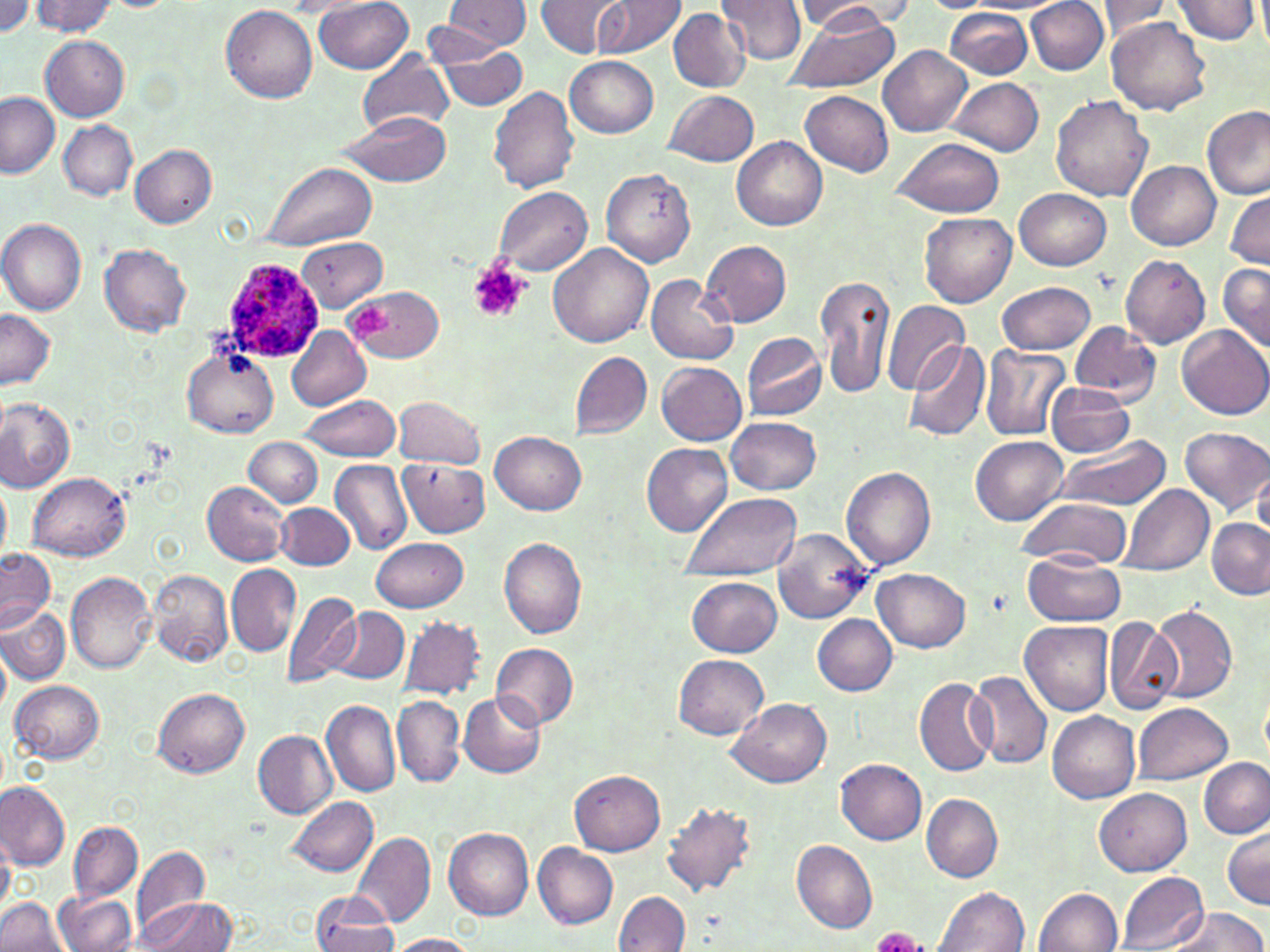
Summary:
  - Coordinate format: approximate bounding boxes as named x1/y1/x2/y2 corners in pixels
  - Platelet locations: (x1=468, y1=261, x2=530, y2=324), (x1=346, y1=300, x2=392, y2=344), (x1=871, y1=925, x2=927, y2=952)
  - Plasmodium ovale-infected red blood cell locations: (x1=220, y1=255, x2=321, y2=365)
  - Uninfected red blood cell locations: (x1=0, y1=0, x2=34, y2=36), (x1=314, y1=0, x2=413, y2=74), (x1=536, y1=0, x2=629, y2=58), (x1=594, y1=0, x2=684, y2=59), (x1=717, y1=0, x2=808, y2=68), (x1=792, y1=0, x2=915, y2=34), (x1=1027, y1=0, x2=1108, y2=75), (x1=1169, y1=0, x2=1263, y2=45), (x1=30, y1=1, x2=124, y2=37), (x1=441, y1=1, x2=533, y2=50), (x1=925, y1=1, x2=991, y2=13), (x1=1093, y1=2, x2=1176, y2=39), (x1=220, y1=5, x2=317, y2=104), (x1=668, y1=9, x2=752, y2=92), (x1=780, y1=10, x2=899, y2=94), (x1=946, y1=10, x2=1034, y2=80), (x1=1106, y1=16, x2=1210, y2=116), (x1=39, y1=34, x2=129, y2=121), (x1=428, y1=37, x2=530, y2=111), (x1=879, y1=45, x2=972, y2=136), (x1=358, y1=49, x2=452, y2=134), (x1=565, y1=56, x2=658, y2=137), (x1=948, y1=77, x2=1044, y2=156), (x1=489, y1=86, x2=581, y2=194), (x1=664, y1=90, x2=760, y2=167), (x1=802, y1=90, x2=894, y2=176), (x1=0, y1=92, x2=60, y2=179), (x1=1051, y1=95, x2=1152, y2=202), (x1=1200, y1=105, x2=1269, y2=200), (x1=336, y1=110, x2=452, y2=187), (x1=59, y1=122, x2=137, y2=199), (x1=891, y1=135, x2=1005, y2=219), (x1=732, y1=136, x2=829, y2=230), (x1=128, y1=144, x2=217, y2=228), (x1=262, y1=161, x2=377, y2=250), (x1=1128, y1=161, x2=1220, y2=249), (x1=601, y1=167, x2=696, y2=267), (x1=493, y1=187, x2=593, y2=274), (x1=1015, y1=187, x2=1110, y2=270), (x1=1225, y1=189, x2=1270, y2=270), (x1=920, y1=213, x2=1018, y2=308), (x1=0, y1=218, x2=86, y2=316), (x1=295, y1=237, x2=388, y2=313), (x1=700, y1=242, x2=792, y2=327), (x1=100, y1=244, x2=192, y2=337), (x1=548, y1=244, x2=653, y2=347), (x1=1120, y1=255, x2=1211, y2=348), (x1=1218, y1=263, x2=1270, y2=355), (x1=646, y1=273, x2=738, y2=366), (x1=817, y1=274, x2=896, y2=403), (x1=996, y1=282, x2=1098, y2=355), (x1=347, y1=287, x2=444, y2=363), (x1=882, y1=300, x2=970, y2=396), (x1=0, y1=309, x2=54, y2=390), (x1=1070, y1=320, x2=1161, y2=403), (x1=286, y1=325, x2=371, y2=410), (x1=1176, y1=325, x2=1270, y2=420), (x1=741, y1=332, x2=827, y2=422), (x1=903, y1=339, x2=992, y2=444), (x1=981, y1=344, x2=1072, y2=441), (x1=183, y1=348, x2=278, y2=436), (x1=568, y1=351, x2=653, y2=441), (x1=657, y1=362, x2=748, y2=446), (x1=1045, y1=382, x2=1134, y2=456), (x1=298, y1=394, x2=402, y2=462), (x1=394, y1=396, x2=485, y2=469), (x1=0, y1=397, x2=75, y2=492), (x1=726, y1=416, x2=822, y2=495), (x1=1179, y1=426, x2=1270, y2=515), (x1=490, y1=431, x2=587, y2=515), (x1=970, y1=436, x2=1070, y2=526), (x1=1051, y1=436, x2=1172, y2=510), (x1=246, y1=437, x2=324, y2=508), (x1=642, y1=442, x2=735, y2=536), (x1=398, y1=458, x2=490, y2=538), (x1=331, y1=459, x2=413, y2=557), (x1=841, y1=466, x2=938, y2=569), (x1=1253, y1=468, x2=1270, y2=540), (x1=28, y1=472, x2=131, y2=560), (x1=1, y1=479, x2=11, y2=560), (x1=202, y1=480, x2=290, y2=566), (x1=1121, y1=485, x2=1212, y2=576), (x1=678, y1=490, x2=801, y2=577), (x1=1016, y1=498, x2=1133, y2=568), (x1=277, y1=504, x2=354, y2=570), (x1=1207, y1=519, x2=1270, y2=600), (x1=777, y1=530, x2=875, y2=626), (x1=371, y1=539, x2=469, y2=612), (x1=499, y1=539, x2=589, y2=639), (x1=1, y1=549, x2=55, y2=631), (x1=1024, y1=553, x2=1124, y2=627), (x1=226, y1=563, x2=302, y2=656), (x1=147, y1=568, x2=233, y2=666), (x1=872, y1=569, x2=971, y2=652), (x1=65, y1=572, x2=158, y2=675), (x1=688, y1=577, x2=783, y2=657), (x1=279, y1=588, x2=363, y2=687), (x1=1149, y1=603, x2=1238, y2=704), (x1=0, y1=607, x2=70, y2=684), (x1=328, y1=607, x2=408, y2=684), (x1=811, y1=613, x2=897, y2=694), (x1=397, y1=615, x2=485, y2=703), (x1=1104, y1=617, x2=1186, y2=713), (x1=1020, y1=622, x2=1115, y2=715), (x1=1, y1=640, x2=11, y2=719), (x1=491, y1=643, x2=579, y2=729), (x1=673, y1=655, x2=769, y2=740), (x1=967, y1=669, x2=1054, y2=769), (x1=913, y1=675, x2=998, y2=776), (x1=11, y1=680, x2=104, y2=763), (x1=151, y1=688, x2=249, y2=777), (x1=459, y1=691, x2=546, y2=778), (x1=392, y1=695, x2=465, y2=786), (x1=728, y1=697, x2=832, y2=788), (x1=320, y1=699, x2=400, y2=797), (x1=1131, y1=702, x2=1233, y2=786), (x1=1047, y1=710, x2=1140, y2=803), (x1=253, y1=730, x2=337, y2=818), (x1=1198, y1=757, x2=1270, y2=840), (x1=837, y1=758, x2=928, y2=844), (x1=570, y1=770, x2=665, y2=856), (x1=0, y1=781, x2=71, y2=872), (x1=1093, y1=786, x2=1191, y2=876), (x1=921, y1=793, x2=1002, y2=881), (x1=285, y1=796, x2=381, y2=878), (x1=661, y1=801, x2=761, y2=898), (x1=69, y1=822, x2=142, y2=903), (x1=1222, y1=825, x2=1269, y2=909), (x1=442, y1=827, x2=534, y2=919), (x1=350, y1=832, x2=435, y2=928), (x1=0, y1=835, x2=14, y2=916), (x1=792, y1=839, x2=878, y2=934), (x1=533, y1=843, x2=619, y2=928), (x1=133, y1=845, x2=210, y2=939), (x1=1117, y1=870, x2=1209, y2=952), (x1=933, y1=886, x2=1031, y2=952), (x1=1035, y1=888, x2=1122, y2=952), (x1=55, y1=890, x2=138, y2=952), (x1=614, y1=891, x2=689, y2=951), (x1=310, y1=893, x2=401, y2=952), (x1=0, y1=897, x2=67, y2=952), (x1=134, y1=898, x2=235, y2=950), (x1=1163, y1=906, x2=1266, y2=952), (x1=386, y1=934, x2=481, y2=952)
  - Slide-level diagnosis: Plasmodium ovale
  - Magnification: 1000x
  - Field of view: single
  - Preparation: thin blood smear
  - Image size: 1270×952 pixels
  - Stain: May-Grünwald-Giemsa
  - Modality: light microscopy